Report the malaria status of this cell.
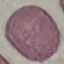
Uninfected.

stain = Giemsa
image type = cell patch, automatically extracted from a larger field of view and resized to 64 × 64 pixels
capture = smartphone camera at the microscope eyepiece
preparation = thin smear